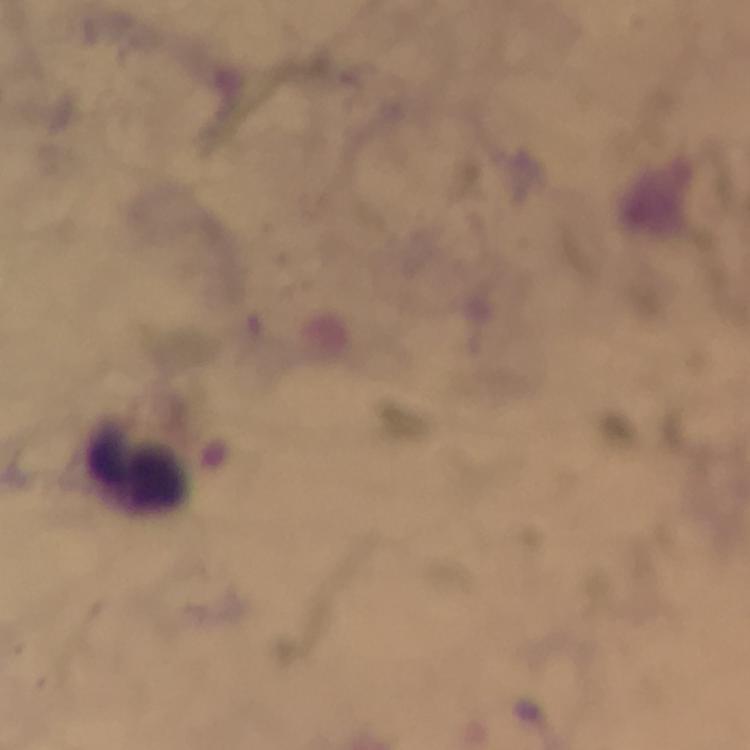

{
  "stain": "Giemsa",
  "preparation": "thick blood smear",
  "immersion_oil": "used",
  "image_size": "750×750 pixels",
  "magnification": "100x",
  "cropped_from": "one field of view",
  "malaria_parasites": "none detected",
  "leukocyte_locations": "approximate centers as {x, y} in pixels: {136, 464}",
  "context": "from a diagnostic examination for malaria",
  "capture": "smartphone camera through the microscope"
}